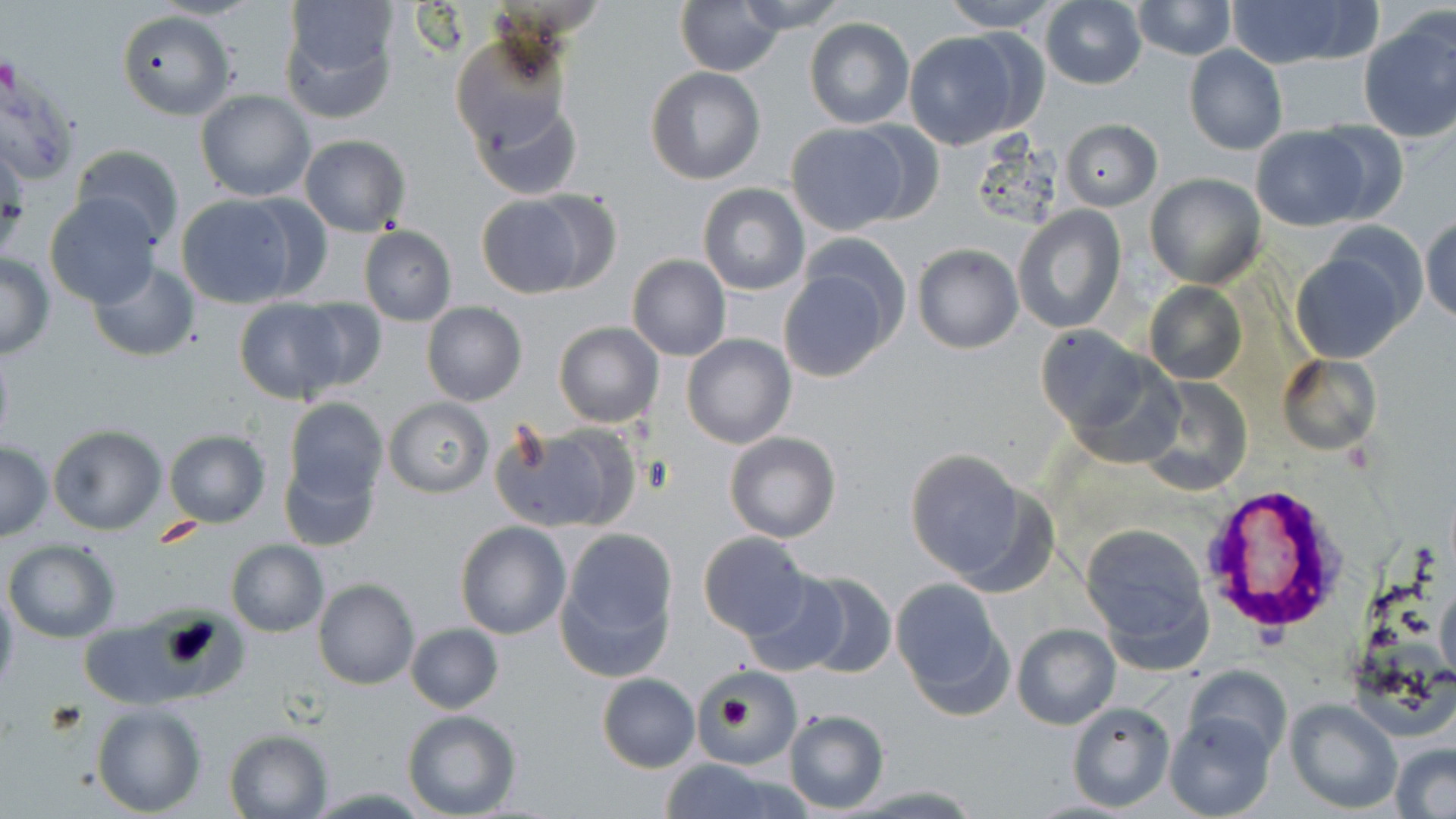

Summary:
  - Coordinate format: approximate bounding boxes as (x1,y1)-(x2,y2) corner pairs in pixels
  - Uninfected red blood cell locations: (280,0)-(402,119), (677,0)-(784,75), (734,0)-(848,30), (937,0)-(1066,32), (1130,0)-(1237,60), (1040,1)-(1147,89), (1222,1)-(1370,69), (117,10)-(233,119), (1358,15)-(1456,144), (804,18)-(915,130), (905,32)-(1027,149), (450,34)-(573,155), (1184,46)-(1287,156), (646,67)-(765,184), (196,90)-(316,203), (472,99)-(583,201), (1061,119)-(1161,210), (786,122)-(912,234), (852,122)-(944,225), (1249,126)-(1372,231), (299,134)-(412,237), (0,138)-(28,258), (71,143)-(185,246), (1145,172)-(1266,289), (698,184)-(809,294), (475,192)-(596,299), (43,193)-(163,307), (173,194)-(305,308), (1013,205)-(1125,333), (1420,215)-(1456,326), (359,226)-(457,325), (797,233)-(912,350), (911,244)-(1023,354), (1291,244)-(1412,363), (0,254)-(54,359), (626,255)-(731,360), (87,261)-(201,362), (776,266)-(896,382), (1144,282)-(1246,385), (233,297)-(354,404), (288,297)-(389,393), (421,302)-(527,404), (554,322)-(664,427), (1035,324)-(1153,440), (682,334)-(795,450), (0,338)-(14,452), (1279,352)-(1384,456), (1136,377)-(1253,495), (284,398)-(387,504), (384,398)-(492,497), (495,424)-(638,534), (46,425)-(167,534), (163,429)-(271,528), (724,431)-(841,542), (0,441)-(51,540), (905,449)-(1034,584), (279,451)-(380,552), (455,521)-(570,639), (1081,523)-(1213,660), (554,526)-(680,681), (698,532)-(812,639), (4,539)-(121,642), (226,540)-(328,637), (795,571)-(897,678), (314,578)-(420,690), (742,579)-(847,676), (890,579)-(1012,716), (0,585)-(19,698), (1435,587)-(1456,677), (78,621)-(188,708), (1012,622)-(1120,729), (405,623)-(503,713), (1188,665)-(1292,762), (703,672)-(803,768), (597,673)-(701,773), (1283,698)-(1403,815), (1067,701)-(1175,813), (90,702)-(207,816), (782,709)-(889,813), (402,710)-(522,819), (1165,710)-(1278,819), (223,729)-(331,818), (1389,743)-(1456,819), (652,756)-(805,818)
  - Plasmodium vivax-infected red blood cell locations: (1201,487)-(1344,639)
  - Slide-level diagnosis: Plasmodium vivax
  - Stain: May-Grünwald-Giemsa
  - Field of view: single
  - Preparation: thin blood smear
  - Image size: 1456×819 pixels
  - Magnification: 1000x
  - Modality: optical microscopy